State which parasite is depicted.
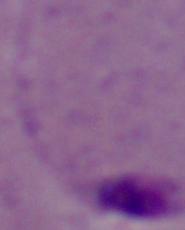

Leishmania.

magnification = 1000x
modality = photomicrograph